Describe the morphology of the red blood cells.
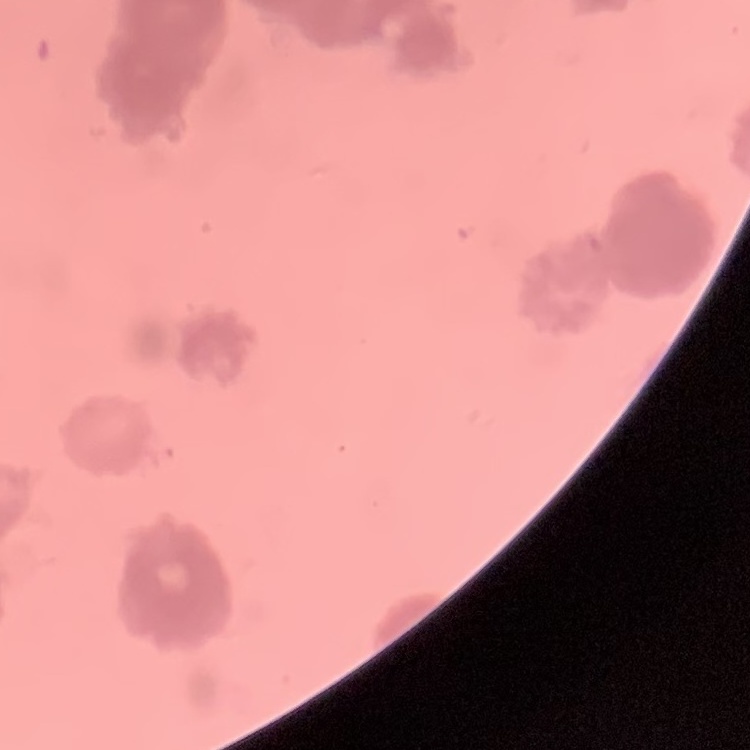
Rouleaux formation.

Square crop of a larger photomicrograph. Thin peripheral smear. Stained with either Field's or Giemsa.